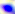

Toxoplasma gondii is seen. 400x magnification. Photomicrograph.